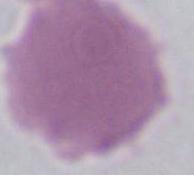
Summary:
  - Modality: micrograph
  - Magnification: 1000x
  - Identification: erythrocyte